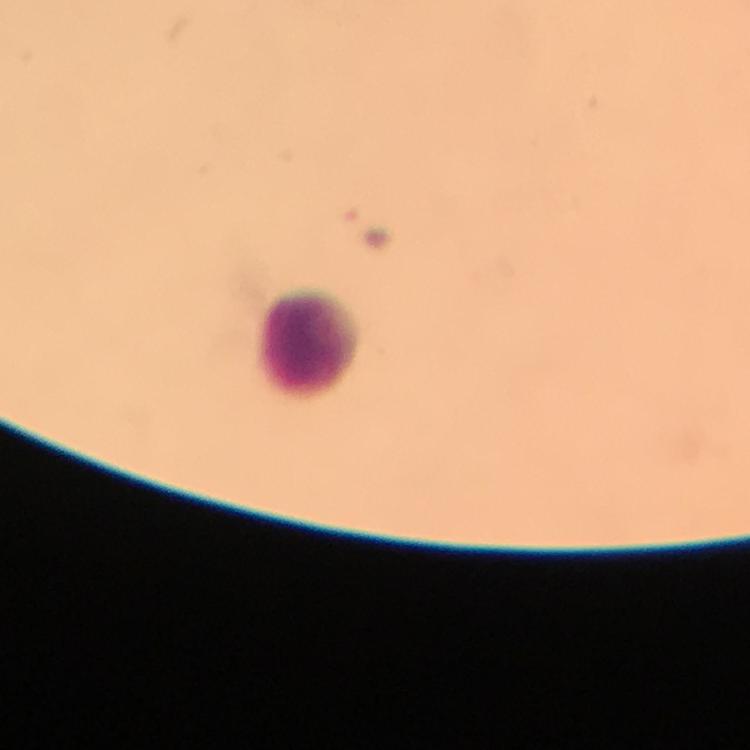 Approximate centers as {x, y} in pixels. Leukocyte locations: {306, 343}. Photographed with a smartphone mounted on the microscope. Malaria parasites: none detected. From a diagnostic examination for malaria. Immersion oil applied. At 100x magnification. Thick blood film. Cropped region of a single field of view. Image is 750×750 pixels. Giemsa-stained preparation.